Name the parasite shown.
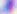

Toxoplasma gondii.

modality = micrograph
magnification = 400x